Point out each Plasmodium parasite.
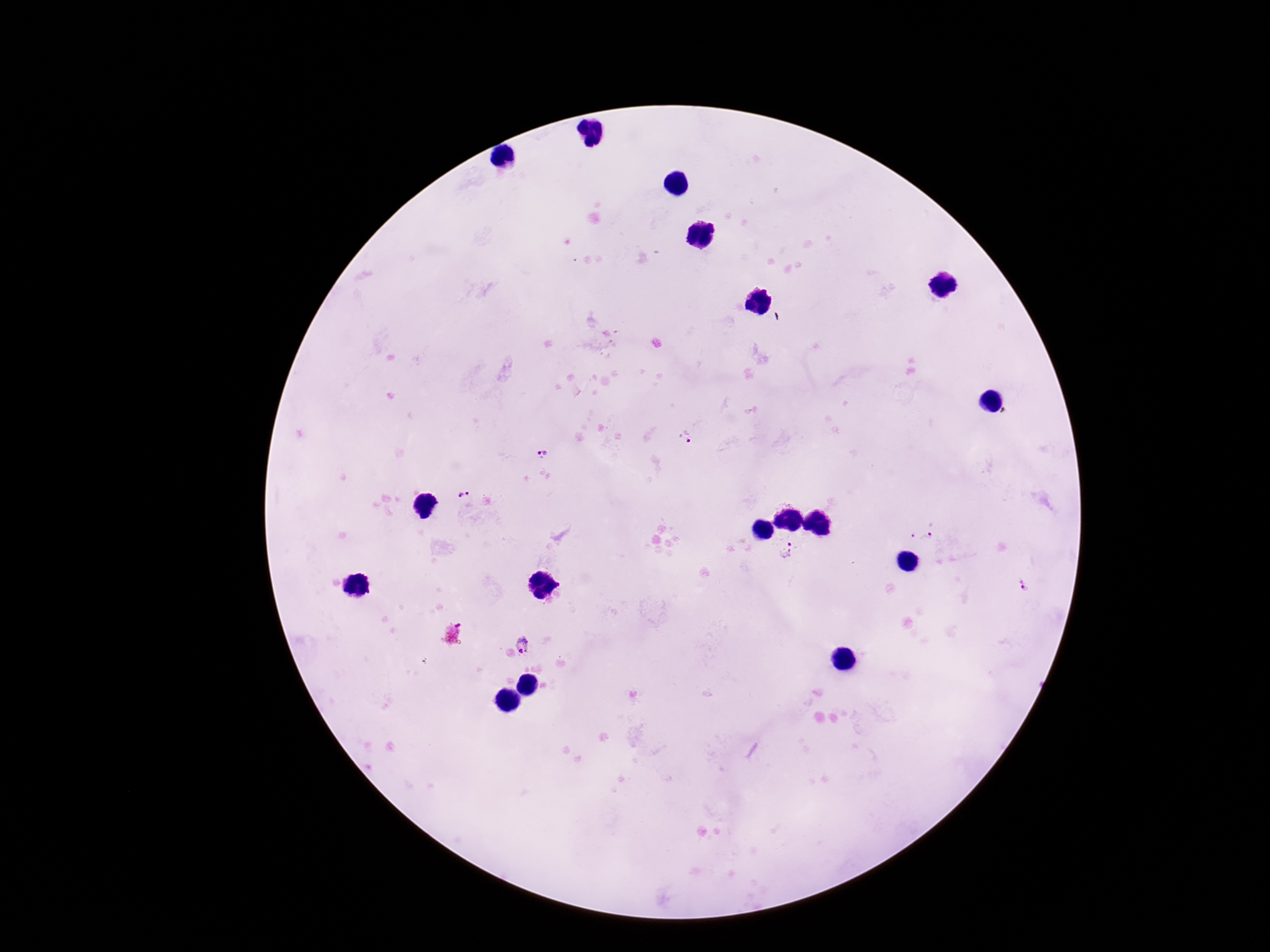

Approximate centers as {x, y} in pixels.
Plasmodium parasites: {685, 438}, {541, 449}, {464, 495}, {912, 534}, {929, 536}, {787, 551}, {1023, 586}, {523, 647}.

capture: smartphone camera through the microscope eyepiece
preparation: thick blood film
image_size: 1270×952 pixels
patient_malaria_status: positive
field_of_view: single
stain: Giemsa
magnification: 100x